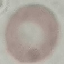
Malaria status: uninfected. Giemsa stain. Acquired by smartphone through the microscope eyepiece. Cell patch, automatically extracted from a larger field of view and resized to 64 × 64 pixels. Thin blood film.